Classify this cell by malaria status.
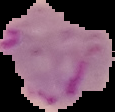
It is parasitized.

Image is 115×112 pixels. Cell region segmented out of the field of view; the surrounding area is masked to black. From a thin blood smear.